Outline each Plasmodium falciparum-infected red blood cell.
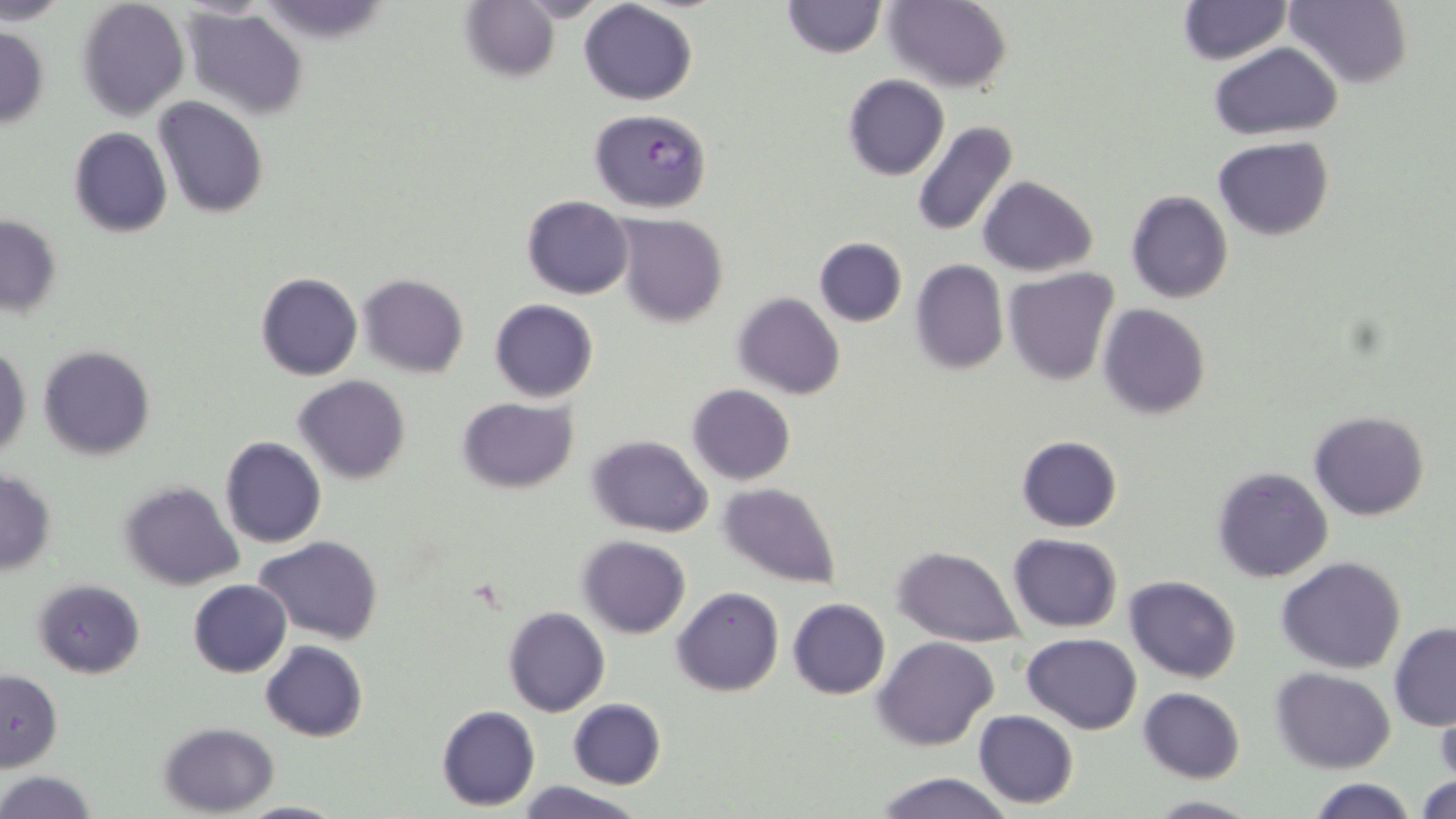

Approximate bounding boxes as (x1,y1)-(x2,y2) corner pairs in pixels.
Plasmodium falciparum-infected red blood cells: (588,109)-(713,213).

Uninfected red blood cell locations: (0,0)-(70,24), (782,0)-(886,59), (883,0)-(1013,94), (1177,0)-(1291,63), (1286,0)-(1413,88), (76,1)-(189,118), (579,2)-(699,104), (459,3)-(563,84), (183,5)-(308,118), (0,25)-(50,129), (1210,43)-(1343,141), (842,74)-(949,181), (153,96)-(269,219), (910,122)-(1018,239), (68,126)-(173,238), (1214,138)-(1333,239), (977,176)-(1097,277), (1125,190)-(1234,304), (522,195)-(634,299), (613,214)-(729,327), (0,215)-(61,316), (813,236)-(907,327), (910,259)-(1007,375), (1002,268)-(1119,385), (255,272)-(363,381), (358,273)-(469,379), (732,292)-(846,400), (489,299)-(598,402), (1096,303)-(1212,419), (0,343)-(31,459), (38,345)-(155,461), (294,374)-(410,485), (687,384)-(796,485), (459,398)-(578,493), (1309,409)-(1430,521), (585,434)-(713,537), (1016,435)-(1123,531), (219,436)-(327,549), (1212,466)-(1334,583), (0,470)-(57,576), (118,481)-(244,590), (718,482)-(843,590), (1008,534)-(1122,631), (576,535)-(691,638), (255,536)-(383,642), (892,545)-(1023,646), (1277,557)-(1407,674), (1124,575)-(1240,683), (34,579)-(145,677), (188,579)-(292,676), (672,587)-(783,697), (787,598)-(890,700), (504,605)-(609,717), (1389,622)-(1456,730), (1023,633)-(1142,733), (874,636)-(1000,750), (260,641)-(369,741), (1271,668)-(1395,774), (1,670)-(63,771), (1137,687)-(1244,784), (567,698)-(667,789), (436,705)-(540,810), (1434,706)-(1456,784), (974,710)-(1078,809), (160,722)-(278,816), (1,771)-(96,818), (870,772)-(1018,818), (1414,773)-(1456,818), (1305,778)-(1417,818), (513,780)-(647,818), (1145,794)-(1258,817), (238,799)-(350,818). Slide-level diagnosis: Plasmodium falciparum. Light microscopy. One field of a larger specimen. Image is 1456×819 pixels. Thin blood smear. Captured at 1000x magnification. May-Grünwald-Giemsa stain.